Give the extent of all uninfected red blood cells.
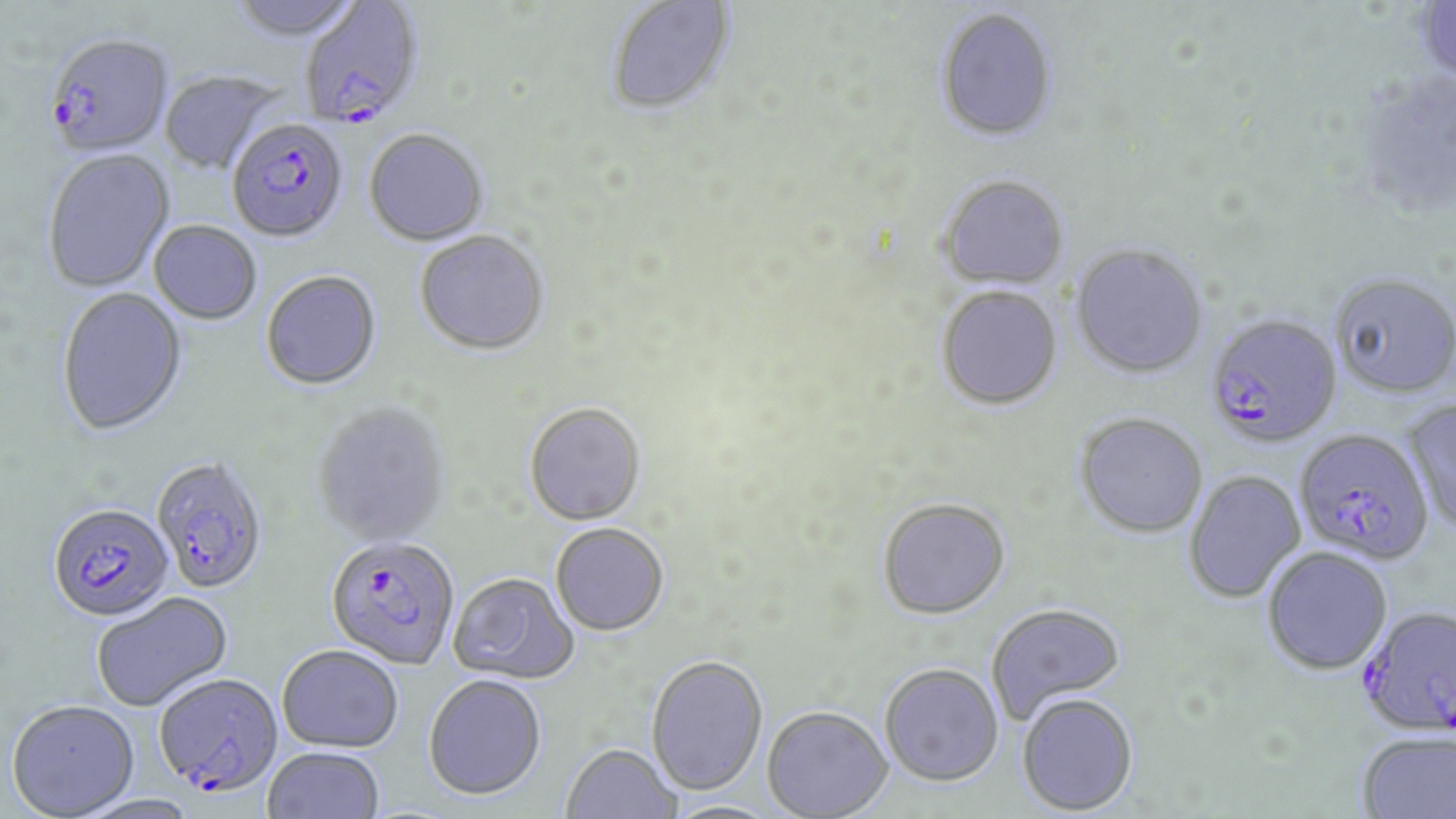

Approximate bounding boxes as (x1,y1)-(x2,y2) corner pairs in pixels.
Uninfected red blood cells: (226,0)-(366,45), (606,1)-(738,118), (1415,1)-(1456,87), (934,8)-(1059,143), (158,71)-(285,176), (364,131)-(488,248), (42,150)-(177,294), (937,175)-(1070,291), (148,222)-(262,326), (414,232)-(549,358), (1070,243)-(1208,379), (261,272)-(382,392), (1329,273)-(1456,398), (936,286)-(1063,411), (56,288)-(188,439), (1404,400)-(1456,534), (312,404)-(452,548), (524,404)-(646,527), (1074,413)-(1208,538), (1183,470)-(1307,602), (876,497)-(1011,620), (551,524)-(669,637), (1261,547)-(1392,674), (448,573)-(580,686), (92,593)-(233,712), (985,602)-(1127,725), (277,645)-(403,752), (645,656)-(768,797), (879,664)-(1004,788), (423,674)-(547,800), (1016,694)-(1139,816), (6,700)-(140,819), (762,707)-(893,819), (1355,732)-(1456,819), (560,744)-(684,818), (262,746)-(386,819).

slide-level diagnosis = Plasmodium falciparum
modality = light microscopy
Plasmodium falciparum-infected red blood cell locations = approximate bounding boxes as (x1,y1)-(x2,y2) corner pairs in pixels: (299,2)-(425,133), (44,37)-(173,160), (227,121)-(349,245), (1204,313)-(1342,448), (1294,429)-(1435,565), (151,458)-(269,595), (48,504)-(175,623), (326,536)-(460,670), (1357,605)-(1456,737), (153,672)-(284,800)
stain = May-Grünwald-Giemsa
preparation = thin blood film
field of view = one of a larger specimen
magnification = 1000x
image size = 1456×819 pixels